Assess this cell for malaria.
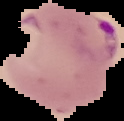
It is parasitized.

preparation = thin blood smear
image size = 124×121 pixels
image type = segmented cell region on a black background